Give the position of every Plasmodium parasite.
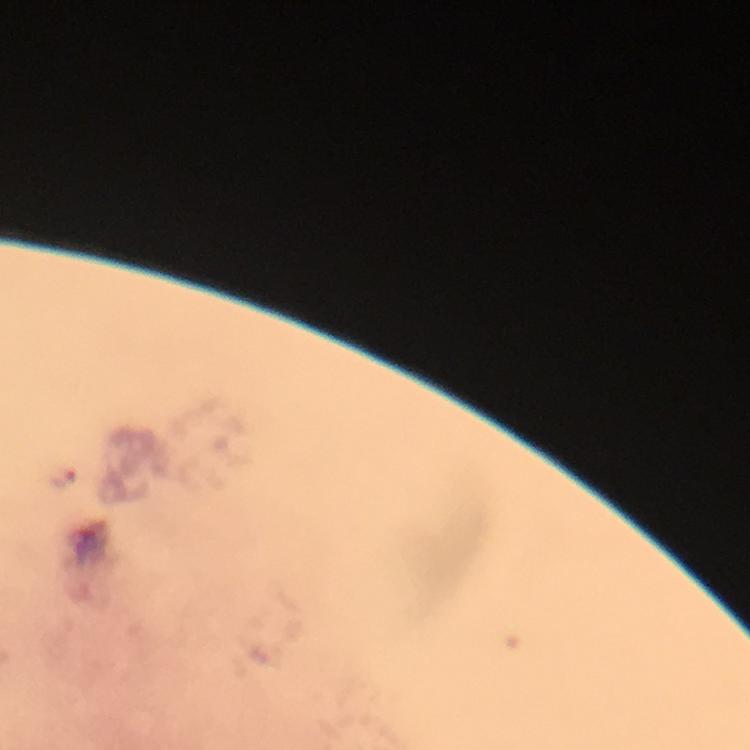
Approximate centers as (x, y) in pixels.
Plasmodium parasites: (62, 477).

A crop from one field of view. Immersion oil was used. From a diagnostic examination for malaria. Thick blood smear. Image is 750×750 pixels. Photographed through the microscope with a smartphone camera. At 100x magnification. Giemsa-stained preparation.